Locate and identify every blood parasite.
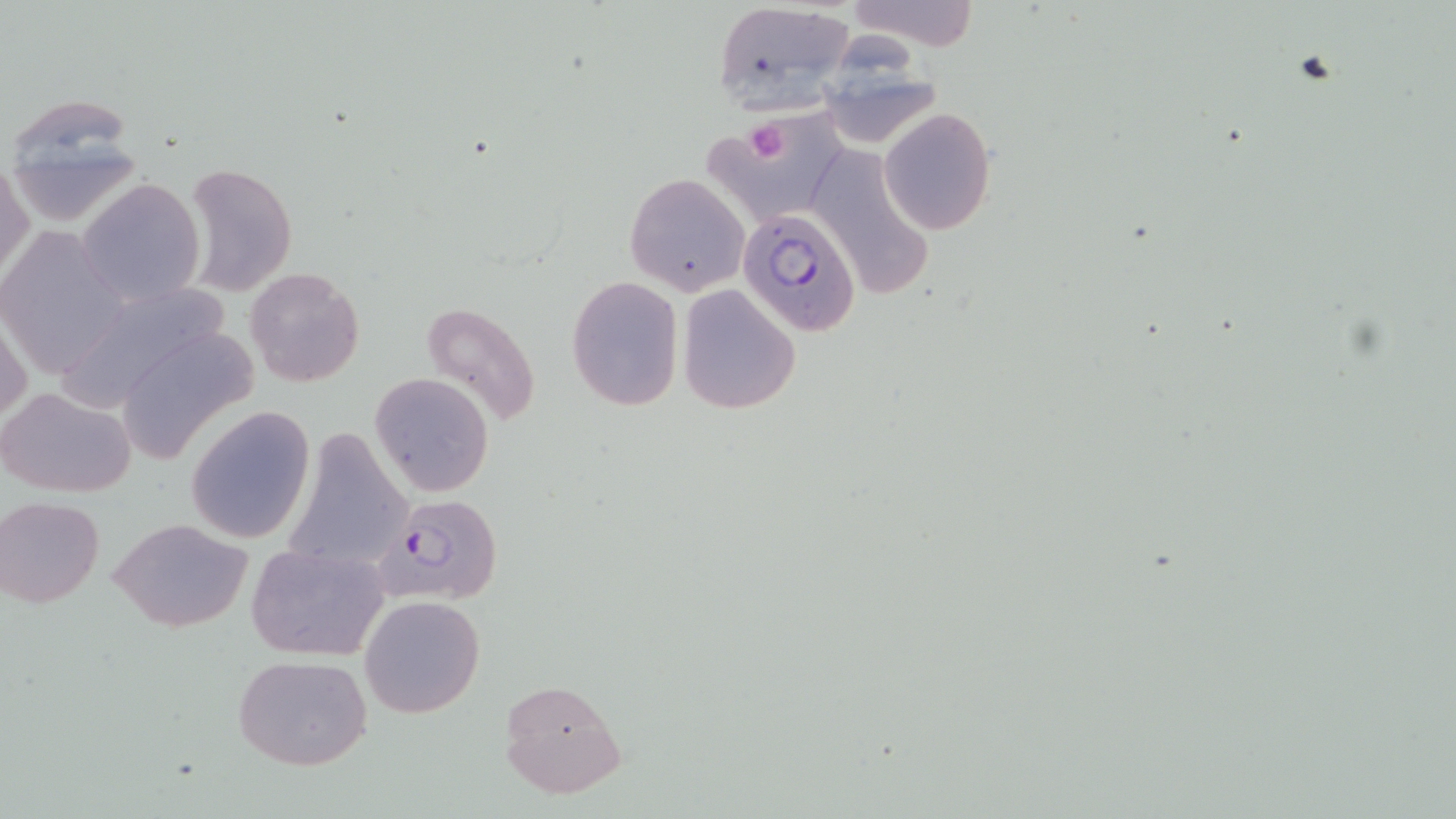
Approximate bounding boxes as [x1, y1, x2, y2] in pixels.
Plasmodium falciparum-infected red blood cells: [738, 208, 862, 338], [378, 493, 503, 604].
No Plasmodium ovale, Plasmodium malariae, Plasmodium vivax, Babesia divergens, or Trypanosoma brucei observed.

Summary:
  - Uninfected red blood cell locations: [845, 0, 982, 51], [710, 1, 857, 114], [816, 48, 943, 148], [2, 95, 146, 225], [706, 102, 847, 218], [879, 108, 996, 233], [809, 144, 931, 295], [1, 161, 33, 285], [182, 161, 296, 296], [625, 172, 750, 297], [78, 179, 206, 307], [0, 229, 124, 378], [245, 267, 364, 388], [566, 276, 684, 412], [53, 278, 236, 412], [677, 284, 801, 415], [423, 302, 542, 428], [1, 313, 31, 429], [112, 324, 260, 463], [369, 373, 494, 496], [0, 385, 136, 498], [185, 406, 316, 544], [282, 426, 413, 578], [1, 497, 104, 606], [109, 518, 254, 633], [246, 543, 389, 662], [360, 594, 486, 720], [233, 654, 372, 771], [497, 679, 626, 800]
  - Platelet locations: [745, 122, 791, 165]
  - Slide-level diagnosis: Plasmodium falciparum
  - Modality: optical microscopy
  - Stain: May-Grünwald-Giemsa
  - Magnification: 1000x
  - Image size: 1456×819 pixels
  - Preparation: thin blood smear
  - Field of view: one of a larger specimen